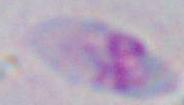

Toxoplasma gondii is seen. 1000x magnification. Micrograph.